Comment on the morphology of the erythrocytes.
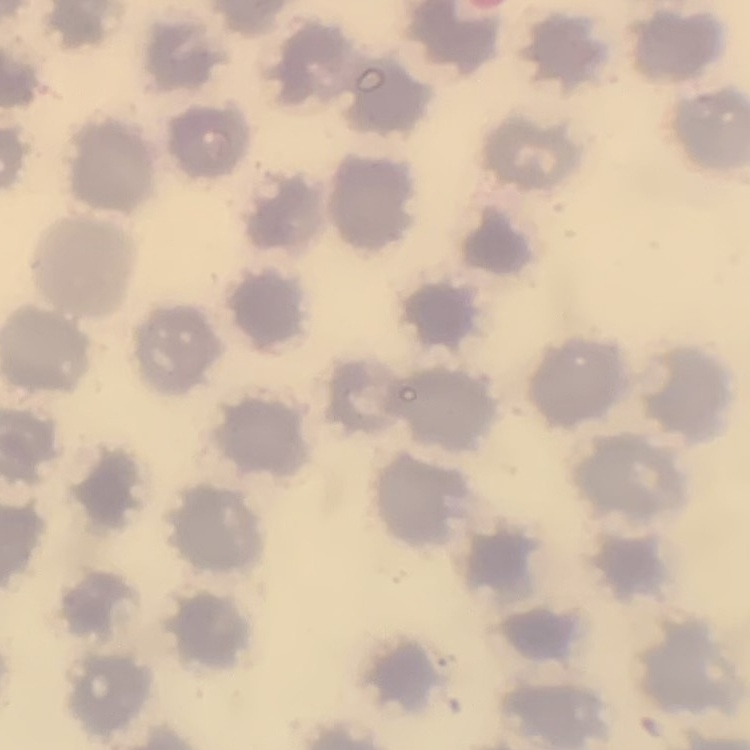

They show no rouleaux formation.

Summary:
  - Image type: one tile cut from a larger photomicrograph
  - Preparation: thin blood film
  - Stain: Field's or Giemsa